Give the extent of all Plasmodium falciparum-infected red blood cells.
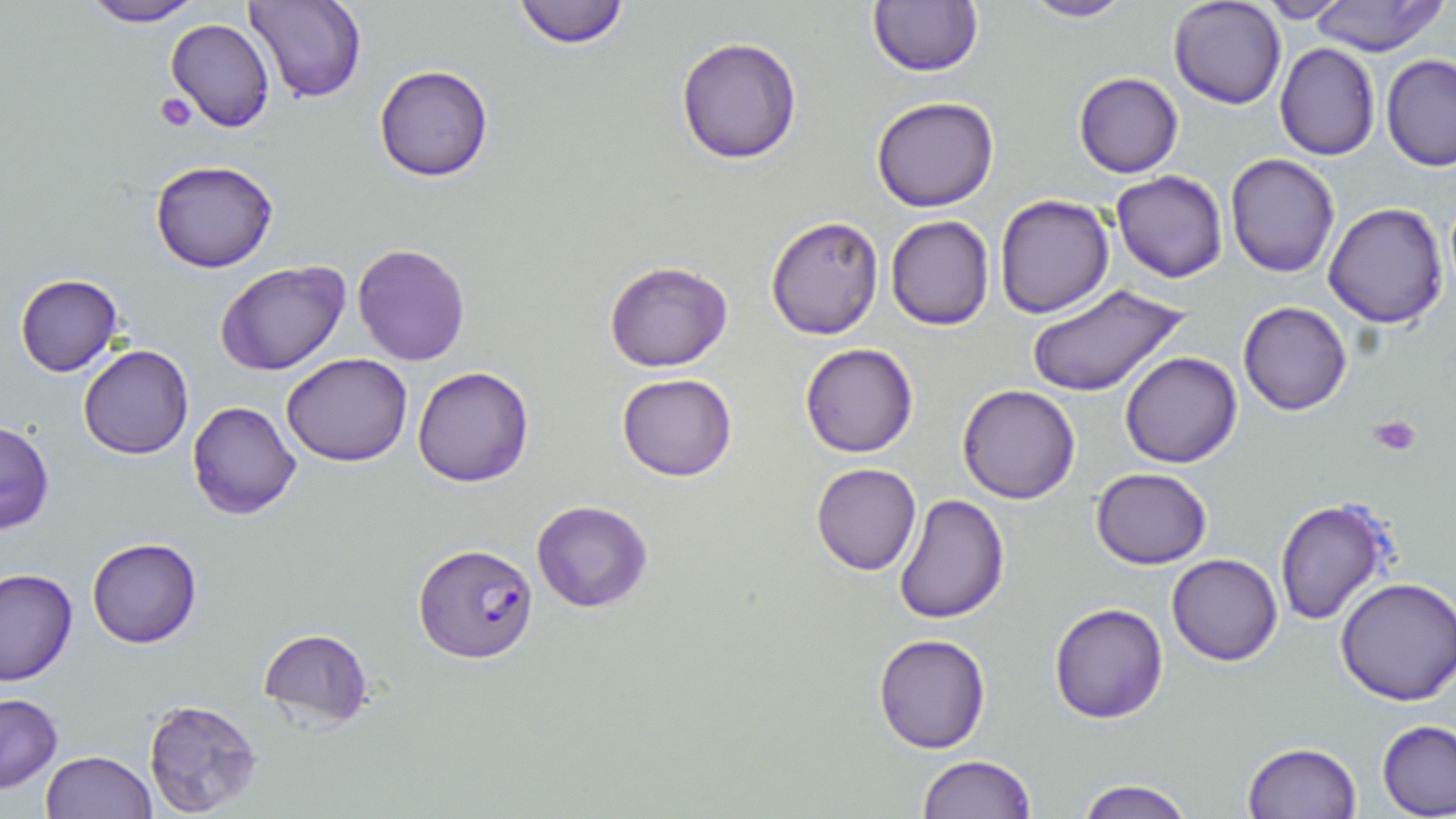

Approximate bounding boxes as named x1/y1/x2/y2 corners in pixels.
Plasmodium falciparum-infected red blood cells: (x1=414, y1=541, x2=539, y2=664).

Platelet locations: (x1=155, y1=94, x2=196, y2=132), (x1=1368, y1=415, x2=1422, y2=456). Uninfected red blood cell locations: (x1=511, y1=0, x2=632, y2=50), (x1=1018, y1=0, x2=1137, y2=23), (x1=1168, y1=0, x2=1287, y2=110), (x1=1253, y1=0, x2=1354, y2=23), (x1=76, y1=1, x2=207, y2=27), (x1=242, y1=1, x2=367, y2=105), (x1=1306, y1=1, x2=1446, y2=55), (x1=867, y1=2, x2=983, y2=77), (x1=165, y1=19, x2=276, y2=134), (x1=675, y1=35, x2=803, y2=164), (x1=1274, y1=42, x2=1381, y2=161), (x1=1381, y1=54, x2=1456, y2=171), (x1=373, y1=64, x2=495, y2=182), (x1=1074, y1=72, x2=1183, y2=177), (x1=872, y1=96, x2=998, y2=212), (x1=1224, y1=154, x2=1339, y2=278), (x1=149, y1=158, x2=278, y2=274), (x1=1110, y1=169, x2=1228, y2=284), (x1=993, y1=193, x2=1115, y2=319), (x1=1324, y1=201, x2=1450, y2=329), (x1=885, y1=214, x2=996, y2=331), (x1=765, y1=215, x2=885, y2=339), (x1=352, y1=243, x2=472, y2=367), (x1=214, y1=260, x2=351, y2=376), (x1=603, y1=260, x2=733, y2=372), (x1=14, y1=274, x2=123, y2=377), (x1=1027, y1=283, x2=1190, y2=398), (x1=1238, y1=300, x2=1352, y2=416), (x1=800, y1=343, x2=919, y2=458), (x1=79, y1=344, x2=194, y2=460), (x1=1120, y1=351, x2=1243, y2=467), (x1=281, y1=353, x2=413, y2=466), (x1=412, y1=365, x2=534, y2=487), (x1=617, y1=373, x2=737, y2=482), (x1=957, y1=383, x2=1082, y2=504), (x1=186, y1=400, x2=303, y2=519), (x1=0, y1=419, x2=54, y2=534), (x1=810, y1=462, x2=922, y2=576), (x1=1090, y1=467, x2=1210, y2=569), (x1=894, y1=492, x2=1011, y2=625), (x1=1275, y1=498, x2=1397, y2=627), (x1=532, y1=500, x2=653, y2=614), (x1=86, y1=537, x2=203, y2=649), (x1=1166, y1=553, x2=1282, y2=667), (x1=0, y1=568, x2=78, y2=686), (x1=1333, y1=576, x2=1456, y2=706), (x1=1048, y1=603, x2=1168, y2=724), (x1=258, y1=627, x2=374, y2=730), (x1=873, y1=633, x2=992, y2=752), (x1=0, y1=692, x2=62, y2=794), (x1=143, y1=698, x2=263, y2=816), (x1=1376, y1=720, x2=1456, y2=818), (x1=1243, y1=741, x2=1363, y2=818), (x1=40, y1=750, x2=156, y2=818), (x1=917, y1=754, x2=1038, y2=818), (x1=1073, y1=778, x2=1198, y2=819). Slide-level diagnosis: Plasmodium falciparum. Single field of view. Light microscopy. 1000x magnification. Image is 1456×819 pixels. May-Grünwald-Giemsa-stained preparation. Thin blood film.